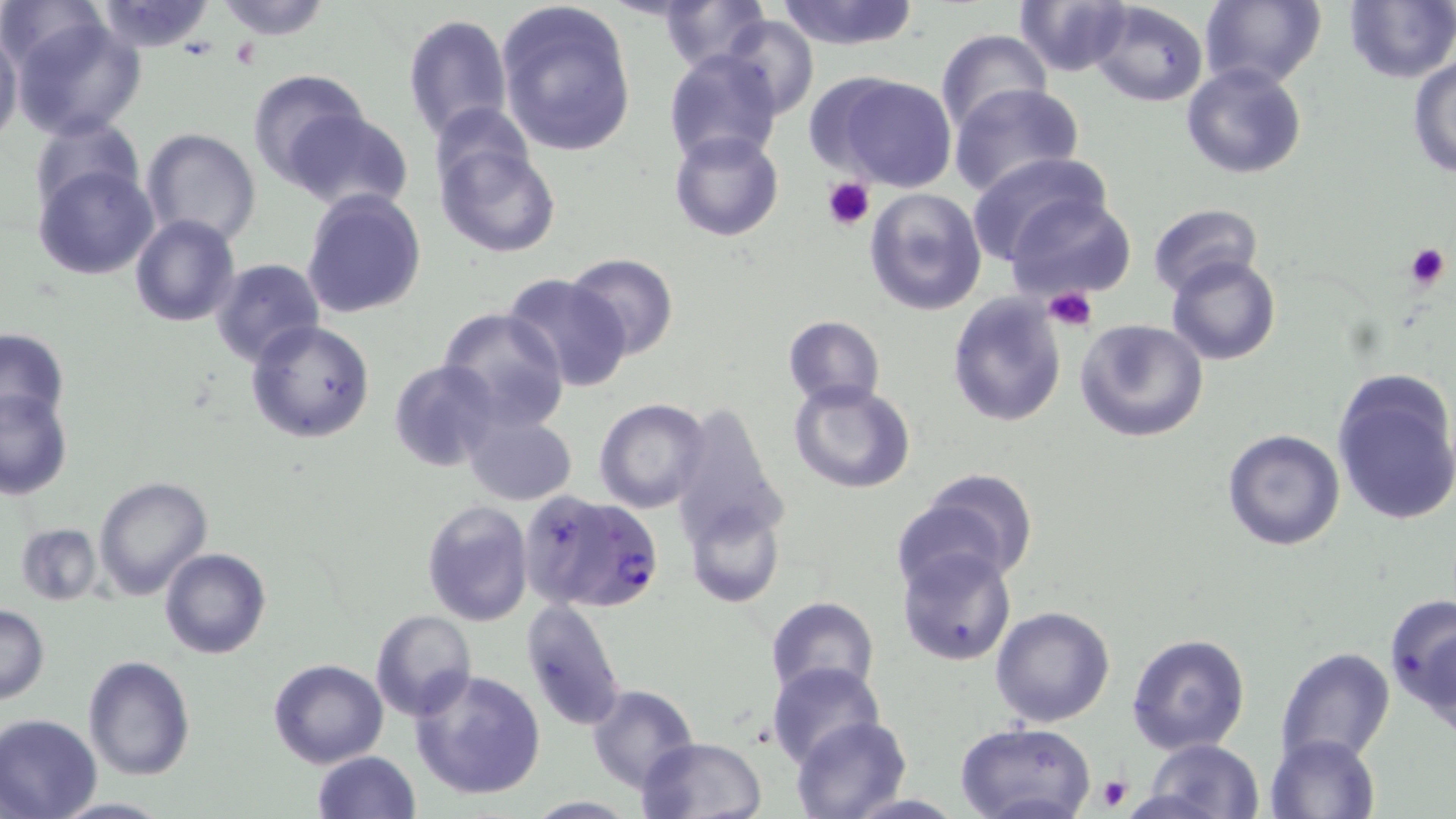

Summary:
  - Coordinate format: approximate bounding boxes as named x1/y1/x2/y2 corners in pixels
  - Platelet locations: (x1=821, y1=176, x2=877, y2=229), (x1=1405, y1=242, x2=1449, y2=292), (x1=1043, y1=288, x2=1097, y2=333), (x1=1096, y1=775, x2=1133, y2=812)
  - Plasmodium falciparum-infected red blood cell locations: (x1=518, y1=490, x2=663, y2=615)
  - Uninfected red blood cell locations: (x1=3, y1=0, x2=106, y2=72), (x1=92, y1=0, x2=220, y2=54), (x1=214, y1=0, x2=333, y2=39), (x1=496, y1=0, x2=637, y2=158), (x1=657, y1=0, x2=769, y2=71), (x1=774, y1=0, x2=923, y2=50), (x1=1015, y1=0, x2=1135, y2=77), (x1=1200, y1=0, x2=1326, y2=91), (x1=1342, y1=0, x2=1455, y2=85), (x1=1088, y1=1, x2=1211, y2=107), (x1=8, y1=10, x2=148, y2=141), (x1=403, y1=14, x2=512, y2=140), (x1=722, y1=16, x2=818, y2=120), (x1=0, y1=22, x2=23, y2=153), (x1=935, y1=30, x2=1051, y2=136), (x1=663, y1=49, x2=783, y2=167), (x1=1407, y1=55, x2=1456, y2=179), (x1=1181, y1=62, x2=1308, y2=182), (x1=248, y1=68, x2=372, y2=191), (x1=819, y1=71, x2=958, y2=192), (x1=949, y1=82, x2=1085, y2=198), (x1=434, y1=104, x2=536, y2=196), (x1=285, y1=109, x2=414, y2=215), (x1=28, y1=116, x2=144, y2=216), (x1=140, y1=127, x2=262, y2=247), (x1=668, y1=132, x2=783, y2=242), (x1=433, y1=135, x2=561, y2=258), (x1=966, y1=151, x2=1114, y2=264), (x1=33, y1=164, x2=160, y2=281), (x1=863, y1=185, x2=989, y2=316), (x1=300, y1=187, x2=427, y2=319), (x1=1005, y1=193, x2=1135, y2=303), (x1=1147, y1=204, x2=1264, y2=299), (x1=131, y1=213, x2=240, y2=327), (x1=565, y1=252, x2=680, y2=359), (x1=1166, y1=255, x2=1281, y2=366), (x1=210, y1=257, x2=325, y2=367), (x1=502, y1=273, x2=631, y2=392), (x1=947, y1=292, x2=1069, y2=427), (x1=437, y1=306, x2=572, y2=429), (x1=781, y1=315, x2=885, y2=410), (x1=247, y1=318, x2=376, y2=443), (x1=1074, y1=318, x2=1208, y2=442), (x1=0, y1=328, x2=70, y2=429), (x1=390, y1=360, x2=504, y2=472), (x1=1331, y1=373, x2=1456, y2=525), (x1=790, y1=381, x2=914, y2=494), (x1=0, y1=388, x2=73, y2=499), (x1=593, y1=399, x2=711, y2=514), (x1=668, y1=402, x2=789, y2=553), (x1=461, y1=406, x2=577, y2=508), (x1=1222, y1=428, x2=1346, y2=550), (x1=903, y1=472, x2=1039, y2=591), (x1=94, y1=476, x2=213, y2=601), (x1=422, y1=500, x2=533, y2=626), (x1=686, y1=503, x2=783, y2=608), (x1=15, y1=522, x2=102, y2=605), (x1=897, y1=544, x2=1017, y2=664), (x1=159, y1=548, x2=270, y2=660), (x1=1384, y1=589, x2=1456, y2=728), (x1=766, y1=596, x2=879, y2=698), (x1=520, y1=599, x2=628, y2=733), (x1=1, y1=604, x2=48, y2=703), (x1=989, y1=606, x2=1116, y2=728), (x1=370, y1=609, x2=477, y2=722), (x1=1126, y1=633, x2=1252, y2=754), (x1=1276, y1=647, x2=1396, y2=767), (x1=84, y1=655, x2=195, y2=779), (x1=267, y1=659, x2=388, y2=769), (x1=766, y1=660, x2=886, y2=770), (x1=408, y1=666, x2=548, y2=800), (x1=586, y1=684, x2=699, y2=792), (x1=0, y1=714, x2=102, y2=819), (x1=789, y1=715, x2=910, y2=818), (x1=955, y1=721, x2=1099, y2=819), (x1=1264, y1=732, x2=1383, y2=819), (x1=637, y1=736, x2=765, y2=819), (x1=1139, y1=739, x2=1266, y2=819), (x1=311, y1=751, x2=421, y2=818), (x1=841, y1=793, x2=967, y2=817), (x1=523, y1=795, x2=637, y2=817), (x1=49, y1=797, x2=171, y2=817)
  - Slide-level diagnosis: Plasmodium falciparum
  - Preparation: thin blood film
  - Field of view: one of a larger specimen
  - Magnification: 1000x
  - Modality: light microscopy
  - Stain: May-Grünwald-Giemsa
  - Image size: 1456×819 pixels